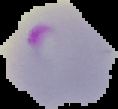 Cell region segmented out of the field of view; the surrounding area is masked to black. Result: malaria parasites detected. Image is 118×109 pixels. From a thin blood smear.